Assess this cell for malaria.
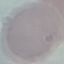
It is uninfected.

capture = smartphone through the microscope eyepiece
image type = cell patch, automatically extracted from a larger field of view and resized to 64 × 64 pixels
preparation = thin smear
stain = Giemsa